Assess this cell for malaria.
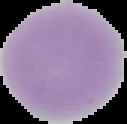

It is uninfected.

Summary:
  - Image size: 127×124 pixels
  - Preparation: thin blood smear
  - Image type: cell region segmented out of the field of view; surrounding area masked to black